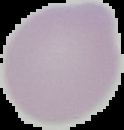

image size = 124×130 pixels
result = no Plasmodium parasites seen
image type = cell region segmented out of the field of view; surrounding area masked to black
preparation = thin blood smear